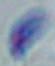
Summary:
  - Identification: Toxoplasma gondii
  - Modality: micrograph
  - Magnification: 1000x